Give the position of every malaria parasite.
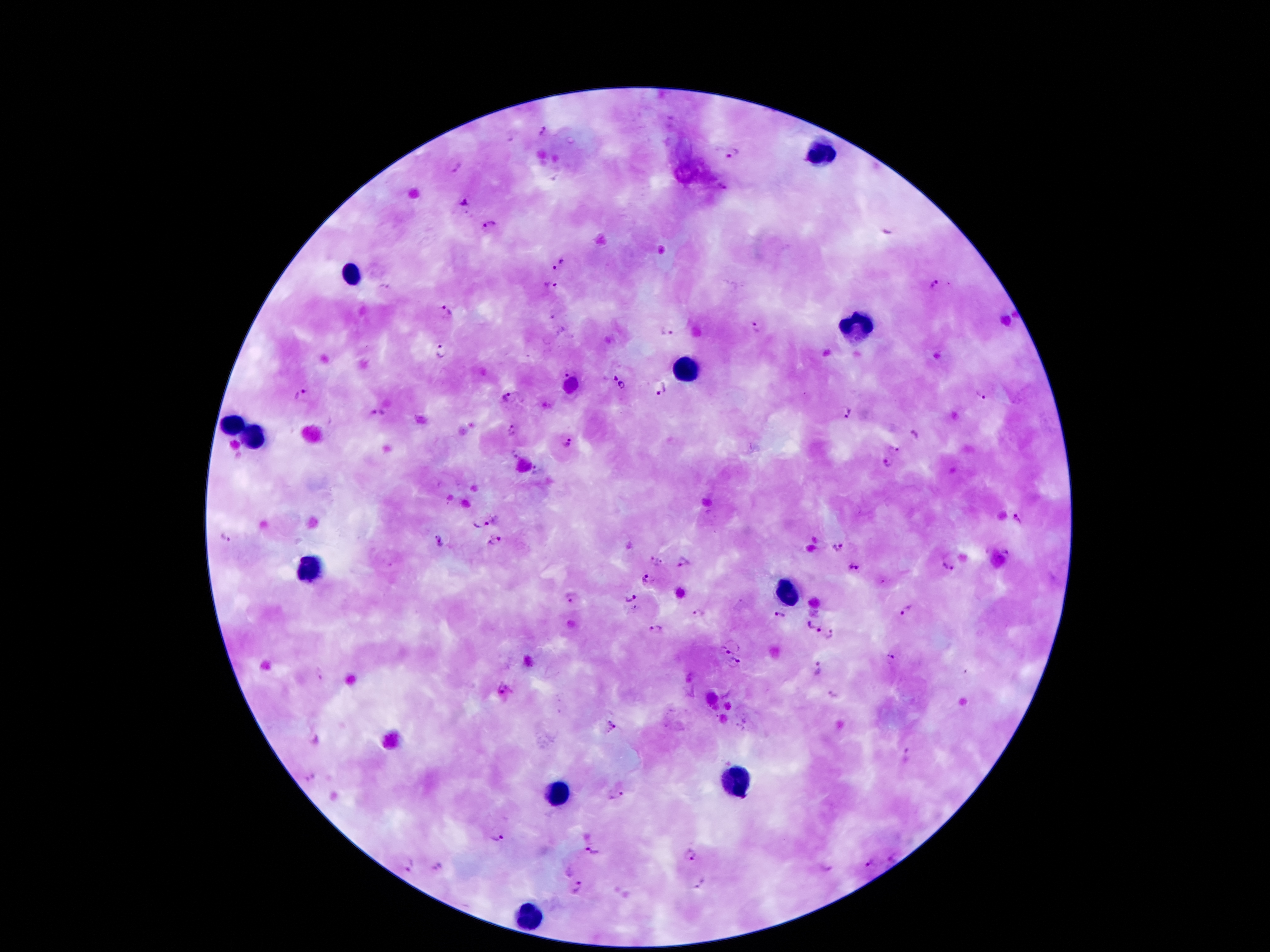
Approximate centers as [x, y] in pixels.
Malaria parasites: [543, 130], [735, 155], [456, 167], [462, 201], [489, 225], [559, 264], [936, 285], [383, 286], [552, 286], [446, 313], [552, 318], [757, 327], [667, 331], [441, 351], [569, 370], [612, 377], [623, 385], [663, 390], [301, 393], [982, 395], [506, 397], [379, 413], [848, 413], [511, 430], [914, 436], [567, 443], [897, 448], [513, 454], [886, 462], [537, 470], [1017, 518], [482, 522], [226, 534], [440, 542], [495, 542], [837, 548], [1007, 554], [657, 559], [682, 564], [947, 566], [853, 567], [649, 580], [569, 597], [633, 598], [906, 609], [634, 610], [697, 614], [779, 615], [811, 625], [655, 629], [830, 636], [721, 650], [890, 658], [736, 663], [818, 671], [319, 674], [503, 688], [831, 694], [612, 725], [907, 755], [309, 778], [614, 796], [497, 837], [592, 850], [691, 855], [893, 857], [869, 864], [437, 865], [407, 866], [826, 869], [699, 884], [576, 888].

Summary:
  - Leukocyte locations: [820, 156], [346, 277], [851, 332], [685, 373], [234, 422], [254, 438], [307, 567], [783, 594], [738, 780], [557, 791], [527, 914]
  - Stain: Giemsa
  - Magnification: 100x
  - Image size: 1270×952 pixels
  - Patient malaria status: infected with Plasmodium falciparum
  - Capture: smartphone camera through the microscope eyepiece
  - Preparation: thick peripheral-blood smear
  - Field of view: single